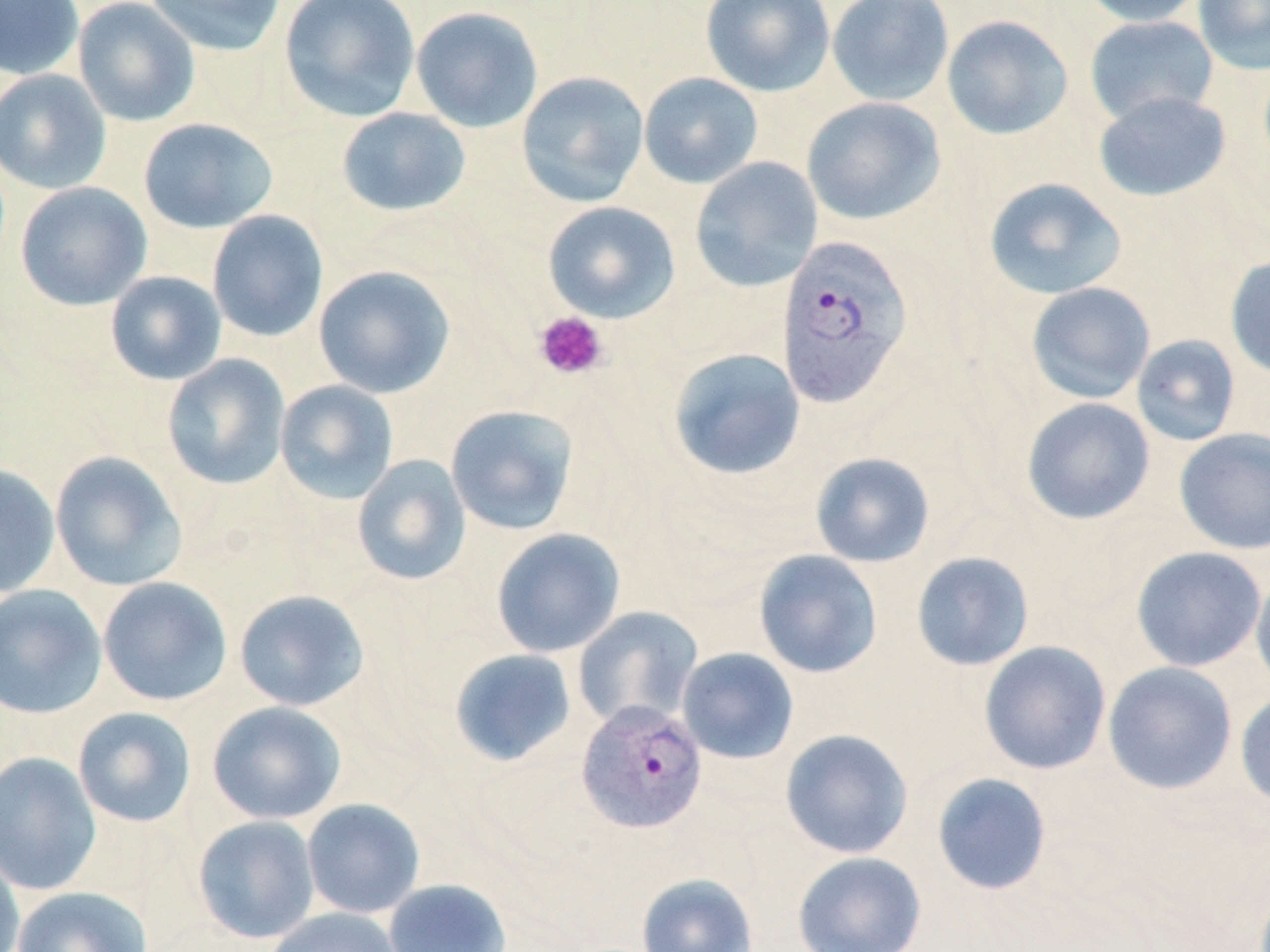
Summary:
  - Coordinate format: approximate bounding boxes as (x1, y1, x2, y2) in pixels
  - Platelet locations: (534, 311, 609, 380)
  - Uninfected red blood cell locations: (0, 0, 85, 81), (73, 0, 200, 127), (143, 0, 287, 57), (279, 0, 422, 123), (700, 0, 835, 97), (827, 0, 954, 107), (1078, 0, 1206, 27), (1192, 0, 1270, 75), (410, 6, 544, 133), (941, 15, 1074, 140), (1084, 15, 1219, 126), (0, 69, 112, 194), (516, 71, 649, 207), (638, 72, 764, 189), (1093, 91, 1232, 202), (801, 97, 946, 225), (336, 107, 471, 217), (138, 117, 279, 234), (690, 156, 824, 293), (984, 177, 1127, 300), (15, 181, 152, 311), (542, 201, 680, 323), (207, 210, 329, 342), (1225, 256, 1270, 380), (313, 265, 456, 398), (105, 271, 227, 386), (1026, 282, 1156, 404), (1131, 334, 1241, 447), (666, 347, 806, 481), (161, 354, 291, 491), (275, 379, 399, 505), (1021, 397, 1155, 525), (445, 404, 579, 535), (1173, 428, 1270, 554), (49, 451, 188, 592), (810, 452, 935, 568), (352, 454, 471, 586), (0, 463, 61, 598), (491, 528, 626, 658), (1130, 546, 1268, 672), (753, 549, 883, 678), (911, 551, 1034, 671), (1250, 569, 1270, 694), (97, 577, 233, 706), (0, 583, 108, 720), (233, 589, 370, 712), (572, 606, 704, 731), (978, 641, 1112, 775), (676, 647, 799, 764), (449, 648, 577, 767), (1102, 661, 1238, 794), (1235, 690, 1270, 811), (206, 701, 347, 825), (72, 706, 197, 828), (780, 728, 913, 859), (0, 751, 102, 896), (931, 772, 1052, 895), (301, 798, 425, 919), (192, 815, 321, 944), (0, 846, 25, 952), (792, 851, 927, 952), (636, 872, 758, 952), (383, 878, 512, 952), (11, 886, 153, 952), (263, 907, 405, 952)
  - Plasmodium vivax-infected red blood cell locations: (775, 235, 915, 409), (576, 700, 708, 834)
  - Slide-level diagnosis: Plasmodium vivax
  - Image size: 1270×952 pixels
  - Modality: light microscopy
  - Preparation: thin blood smear
  - Stain: May-Grünwald-Giemsa
  - Field of view: one of a larger specimen
  - Magnification: 1000x